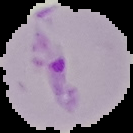
From a thin blood film. Segmented cell region on a black background. Image is 133×133 pixels. Malaria status: parasitized.